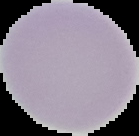

{
  "image_type": "segmented cell region with the area outside set to black",
  "result": "negative for malaria parasites",
  "preparation": "thin blood film",
  "image_size": "139×136 pixels"
}